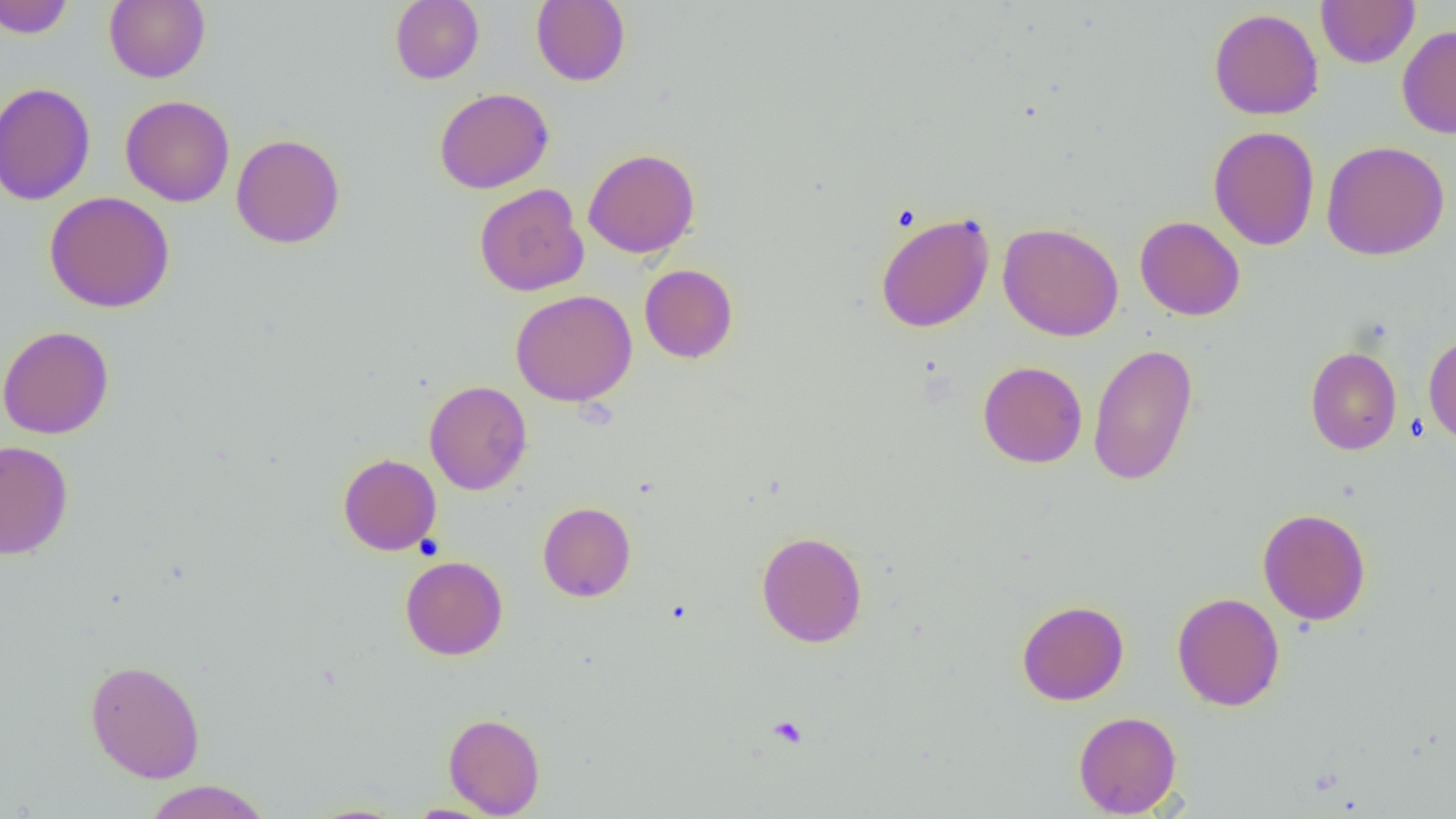

Summary:
  - Coordinate format: approximate bounding boxes as named x1/y1/x2/y2 corners in pixels
  - Uninfected red blood cell locations: (x1=0, y1=0, x2=74, y2=38), (x1=104, y1=0, x2=210, y2=83), (x1=390, y1=0, x2=484, y2=84), (x1=531, y1=0, x2=631, y2=86), (x1=1316, y1=0, x2=1419, y2=68), (x1=1208, y1=8, x2=1324, y2=120), (x1=1397, y1=24, x2=1456, y2=139), (x1=0, y1=82, x2=96, y2=205), (x1=434, y1=87, x2=554, y2=193), (x1=121, y1=95, x2=235, y2=207), (x1=1208, y1=125, x2=1320, y2=251), (x1=231, y1=134, x2=345, y2=249), (x1=1322, y1=140, x2=1450, y2=261), (x1=583, y1=148, x2=700, y2=259), (x1=474, y1=183, x2=589, y2=297), (x1=44, y1=191, x2=175, y2=313), (x1=875, y1=212, x2=995, y2=333), (x1=1134, y1=216, x2=1246, y2=321), (x1=997, y1=222, x2=1123, y2=341), (x1=640, y1=264, x2=738, y2=363), (x1=511, y1=289, x2=637, y2=406), (x1=0, y1=325, x2=114, y2=439), (x1=1423, y1=332, x2=1456, y2=445), (x1=1088, y1=343, x2=1198, y2=486), (x1=1304, y1=346, x2=1402, y2=455), (x1=978, y1=361, x2=1087, y2=468), (x1=424, y1=380, x2=532, y2=495), (x1=0, y1=440, x2=74, y2=559), (x1=338, y1=453, x2=441, y2=555), (x1=537, y1=502, x2=636, y2=602), (x1=1258, y1=508, x2=1371, y2=625), (x1=756, y1=531, x2=868, y2=648), (x1=400, y1=555, x2=508, y2=660), (x1=1171, y1=592, x2=1285, y2=710), (x1=1016, y1=600, x2=1129, y2=705), (x1=85, y1=659, x2=205, y2=783), (x1=1073, y1=711, x2=1182, y2=818), (x1=443, y1=712, x2=545, y2=817), (x1=142, y1=780, x2=272, y2=819), (x1=300, y1=803, x2=412, y2=819), (x1=405, y1=803, x2=500, y2=818)
  - Platelet locations: (x1=768, y1=715, x2=808, y2=748)
  - Slide-level diagnosis: no evidence of blood parasites
  - Field of view: single
  - Modality: light microscopy
  - Magnification: 1000x
  - Image size: 1456×819 pixels
  - Preparation: thin blood smear